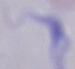
Summary:
  - Modality: photomicrograph
  - Identification: trypanosome
  - Magnification: 1000x